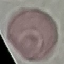
Summary:
  - Malaria status: uninfected
  - Image type: automatically extracted cell patch, resized to 64 × 64 pixels
  - Capture: smartphone camera at the microscope eyepiece
  - Preparation: thin blood film
  - Stain: Giemsa